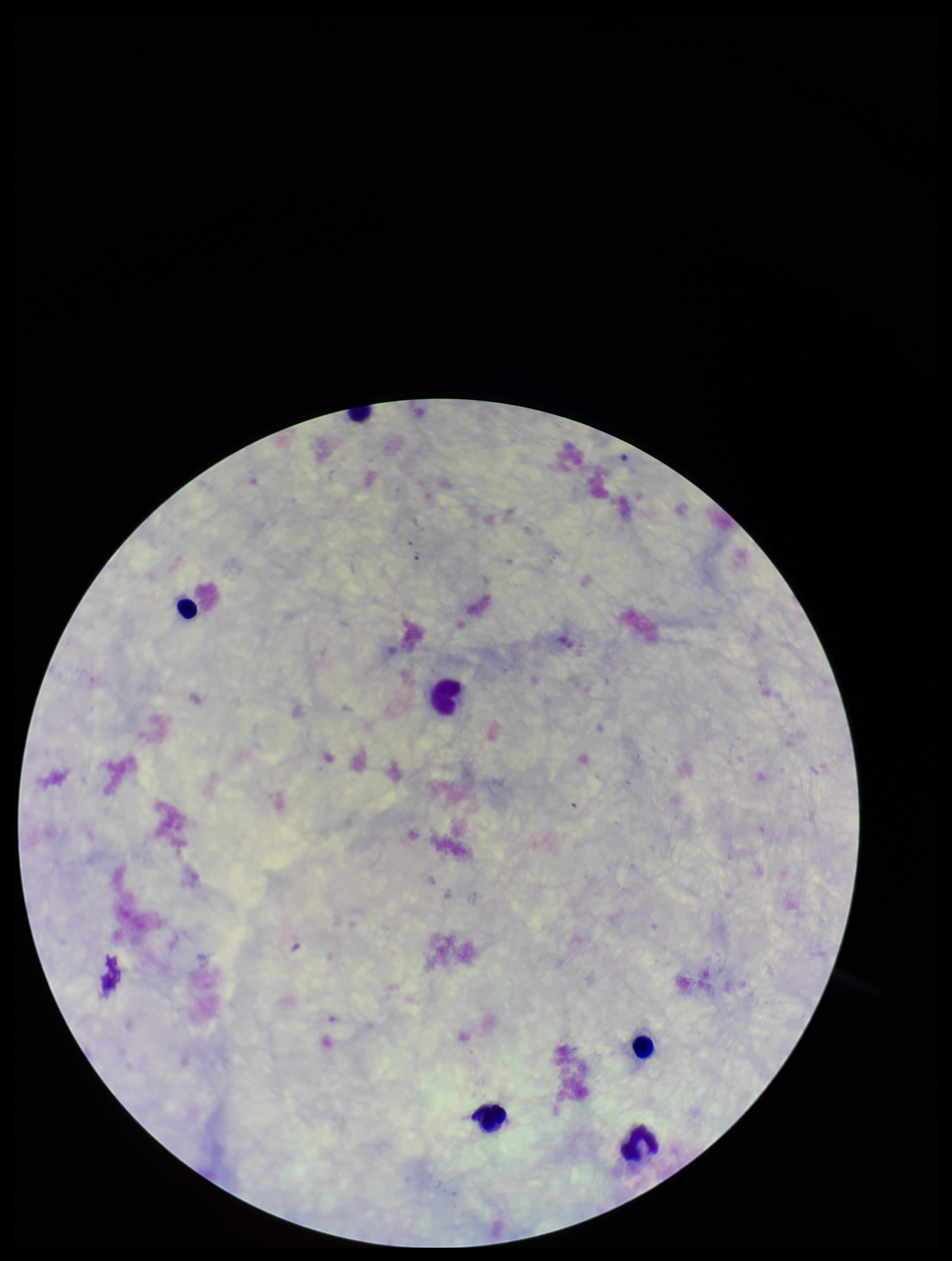
One field from this slide. Image is 952×1261 pixels. Giemsa stain. Patient malaria status: negative. Plasmodium parasites: none identified. Smartphone photograph taken through the eyepiece of a microscope. Leukocyte count: 6. Preparation: thick smear. Parasite count: 0.